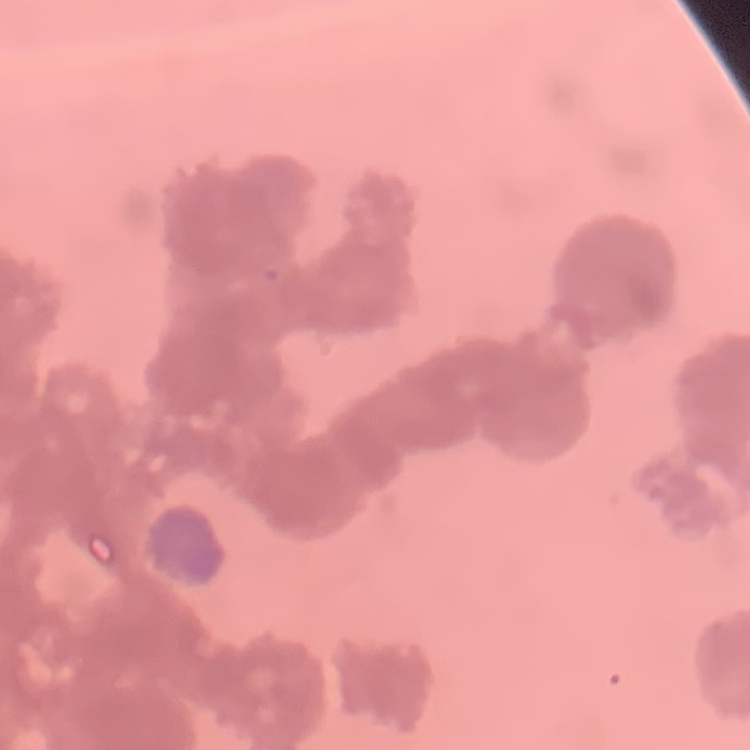
erythrocyte morphology = rouleaux formation
image type = one tile cut from a larger photomicrograph
preparation = thin blood film
stain = Field's or Giemsa